Assess the morphology of the red blood cells.
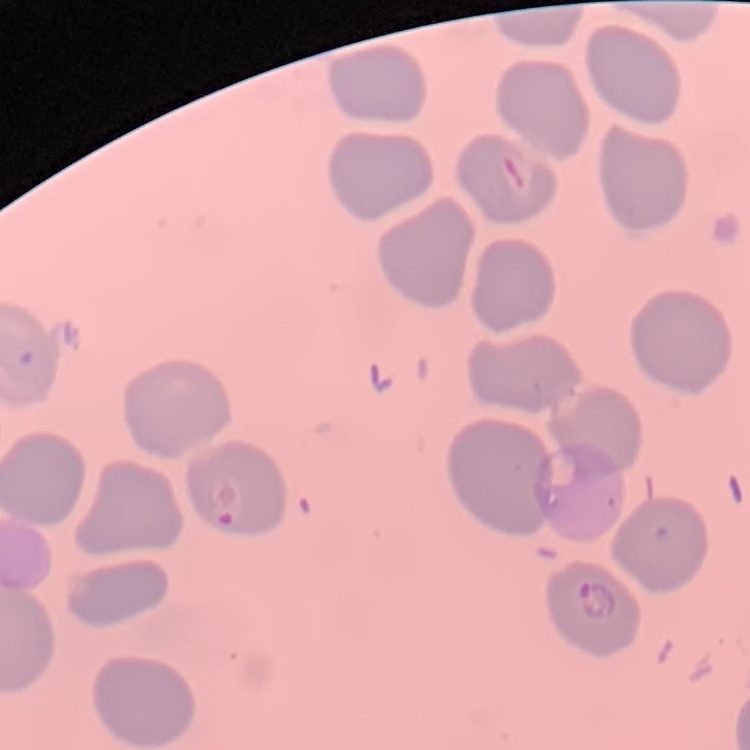

No rouleaux formation.

Summary:
  - Image type: one tile cut from a larger photomicrograph
  - Preparation: thin blood film
  - Stain: Field's or Giemsa